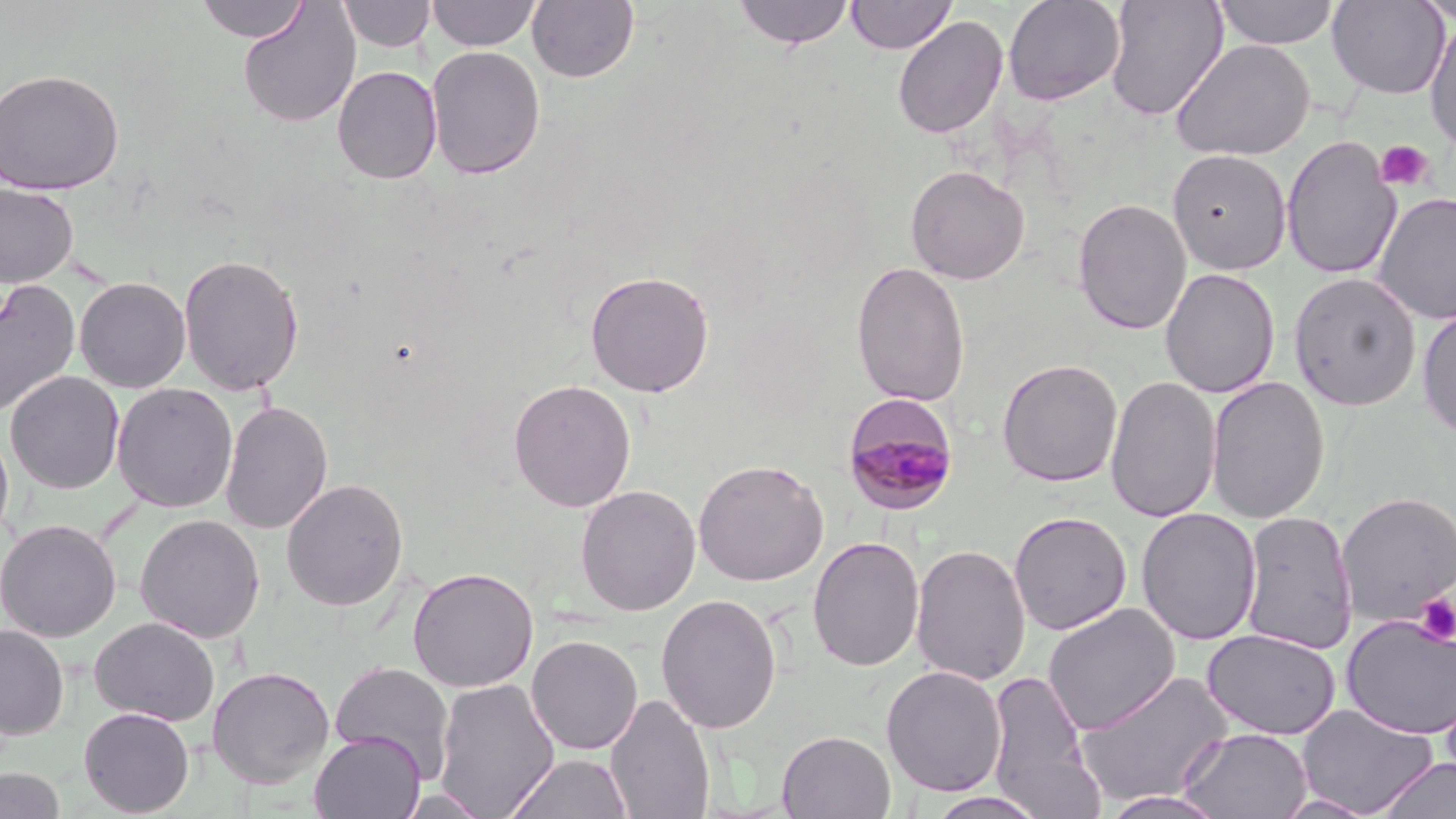 Approximate bounding boxes as [x1, y1, x2, y2] in pixels. Uninfected red blood cell locations: [195, 0, 310, 43], [338, 0, 435, 53], [427, 0, 542, 51], [528, 0, 639, 83], [732, 0, 855, 50], [846, 0, 957, 54], [1002, 0, 1126, 105], [1105, 0, 1228, 120], [1213, 0, 1340, 49], [1327, 0, 1450, 99], [1413, 0, 1456, 26], [237, 3, 361, 128], [893, 15, 1008, 140], [1424, 18, 1456, 157], [1170, 38, 1315, 161], [426, 45, 546, 180], [332, 66, 443, 184], [0, 68, 124, 195], [1281, 135, 1401, 280], [1167, 149, 1292, 274], [905, 164, 1030, 285], [0, 183, 79, 289], [1372, 192, 1456, 325], [1073, 198, 1192, 336], [178, 253, 305, 396], [850, 259, 970, 408], [1160, 268, 1280, 399], [585, 270, 715, 397], [1288, 272, 1422, 411], [75, 277, 191, 393], [0, 279, 80, 420], [1416, 306, 1456, 441], [997, 358, 1123, 487], [5, 371, 125, 494], [1106, 375, 1220, 523], [1206, 375, 1330, 524], [508, 378, 636, 512], [112, 383, 238, 513], [220, 399, 333, 535], [0, 424, 14, 549], [693, 458, 829, 586], [281, 478, 409, 612], [575, 479, 831, 603], [574, 484, 701, 616], [1337, 491, 1456, 629], [1136, 507, 1262, 647], [1240, 509, 1358, 655], [1009, 511, 1132, 634], [134, 514, 266, 643], [1, 519, 121, 642], [807, 536, 925, 672], [911, 543, 1031, 686], [407, 566, 538, 692], [656, 593, 782, 734], [1043, 603, 1180, 736], [1341, 614, 1456, 739], [89, 617, 220, 726], [0, 624, 69, 738], [1202, 629, 1341, 740], [526, 635, 643, 755], [329, 661, 455, 780], [207, 665, 334, 789], [881, 666, 1007, 797], [986, 668, 1101, 817], [1073, 669, 1235, 807], [433, 677, 559, 817], [605, 693, 715, 819], [1295, 704, 1438, 817], [79, 707, 195, 816], [1177, 726, 1312, 819], [310, 730, 426, 819], [778, 730, 895, 818], [505, 753, 633, 819], [1376, 757, 1456, 819], [0, 768, 67, 819], [393, 788, 495, 818], [1098, 790, 1231, 818], [924, 791, 1049, 819]. Platelet locations: [1375, 139, 1435, 192], [1414, 593, 1456, 645]. Plasmodium malariae-infected red blood cell locations: [842, 398, 959, 514]. Slide-level diagnosis: Plasmodium malariae. Light microscopy. May-Grünwald-Giemsa-stained preparation. 1000x magnification. Thin blood smear. Single field of view. Image is 1456×819 pixels.